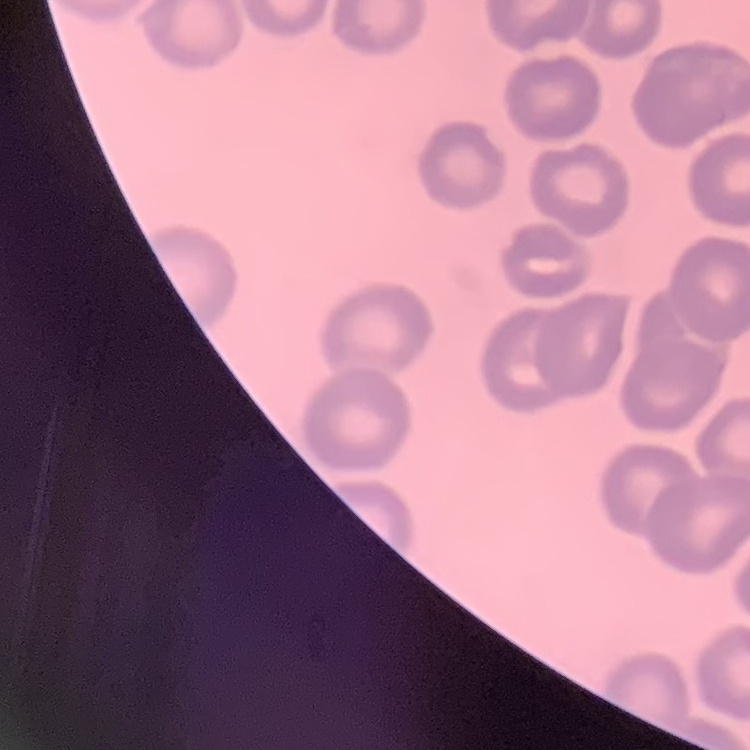
Summary:
  - Erythrocyte morphology: no rouleaux formation
  - Preparation: thin blood film
  - Image type: square crop of a larger photomicrograph
  - Stain: Field's or Giemsa